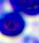

400x magnification. Micrograph. A white blood cell is shown.